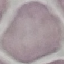
result = negative for malaria parasites
stain = Giemsa
preparation = thin blood smear
capture = smartphone through the microscope eyepiece
image type = cell patch, automatically extracted from a larger field of view and resized to 64 × 64 pixels